Locate every Plasmodium parasite.
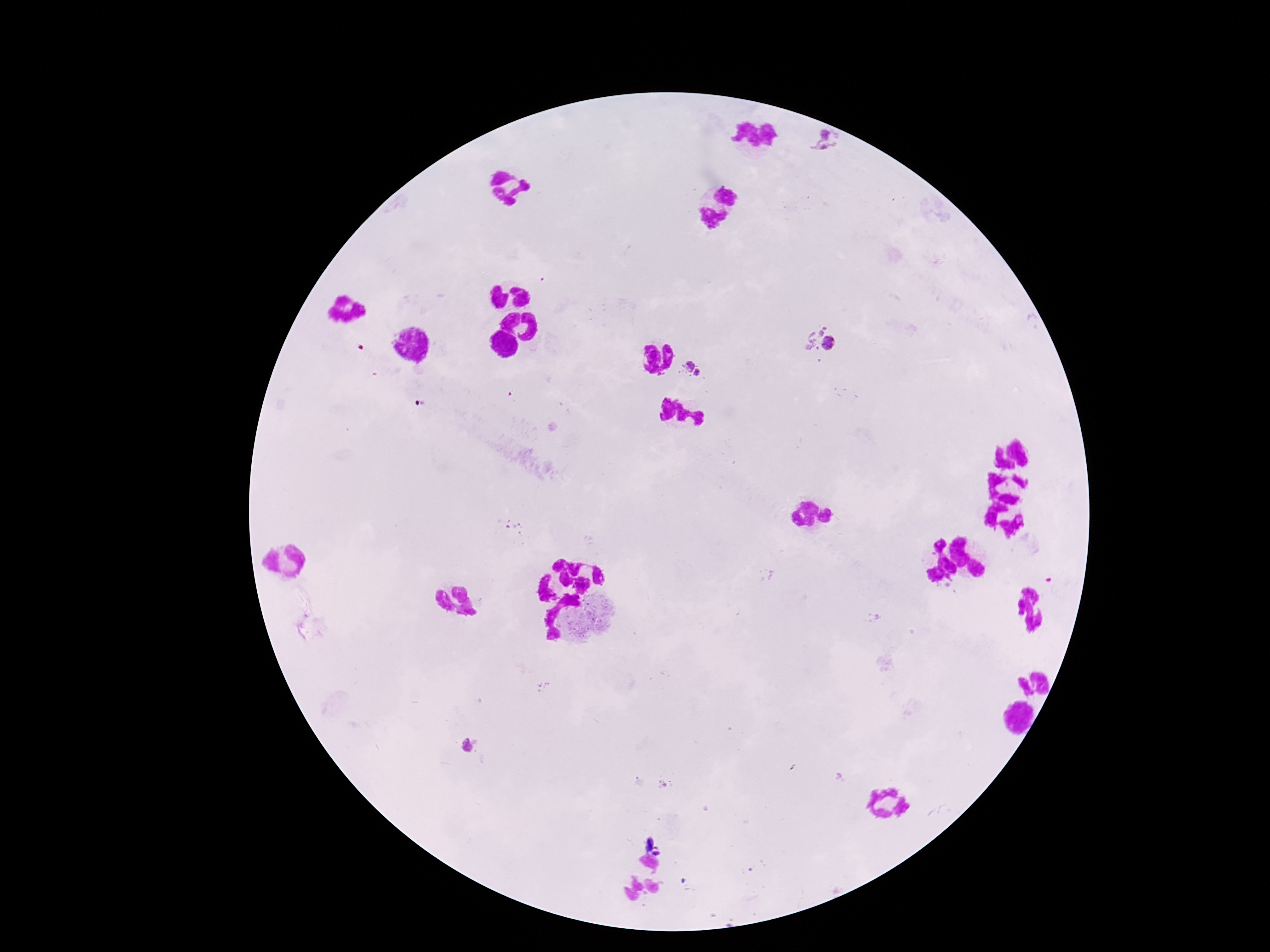

Approximate centers as (x, y) in pixels.
Plasmodium parasites: (827, 144), (808, 333), (830, 344), (688, 365), (698, 373), (468, 746).

Summary:
  - Preparation: thick blood smear
  - Capture: smartphone camera through the microscope eyepiece
  - Image size: 1270×952 pixels
  - Magnification: 100x
  - Stain: Giemsa
  - Field of view: one from this slide
  - Patient malaria status: positive